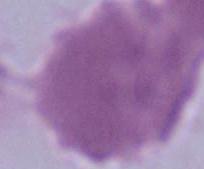

An erythrocyte is shown. Micrograph. Captured at 1000x magnification.